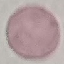

Malaria status: uninfected. Automatically extracted cell patch, resized to 64 × 64 pixels. Giemsa stain. Photographed with a smartphone camera at the microscope eyepiece. Thin blood smear.